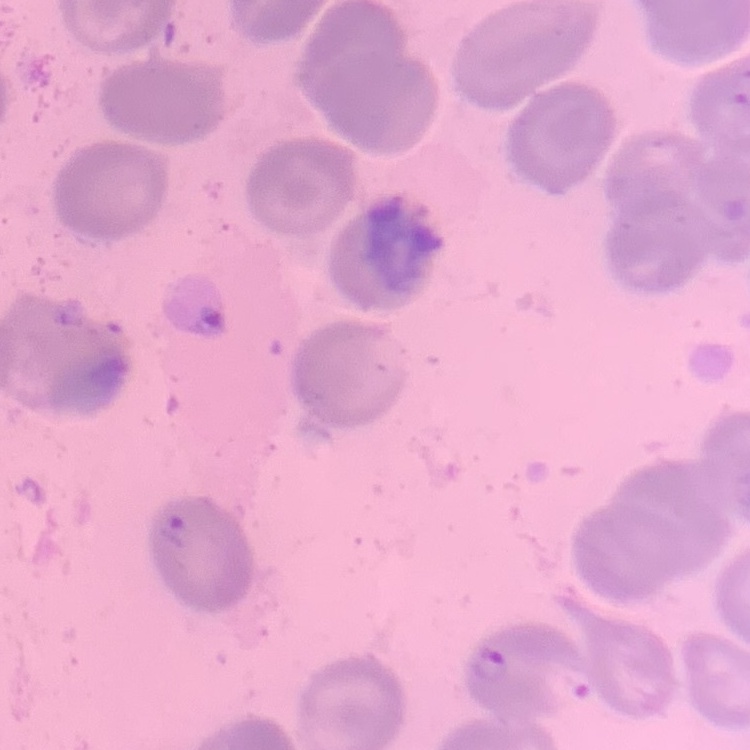

Summary:
  - Red blood cell morphology: no rouleaux formation
  - Image type: one tile cut from a larger photomicrograph
  - Preparation: thin blood smear
  - Stain: Field's or Giemsa